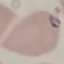
result = malaria parasites detected
preparation = thin blood film
stain = Giemsa
capture = smartphone camera at the microscope eyepiece
image type = cell patch, automatically extracted from a larger field of view and resized to 64 × 64 pixels